State which cell type is depicted.
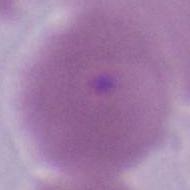
An erythrocyte.

Summary:
  - Modality: photomicrograph
  - Magnification: 1000x